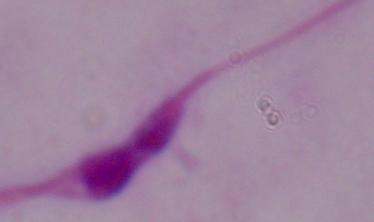

identification = Leishmania
magnification = 1000x
modality = micrograph